Classify this cell by malaria status.
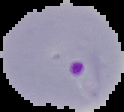
Parasitized.

image_size: 124×112 pixels
image_type: segmented cell region on a black background
preparation: thin blood film